Name the parasite shown.
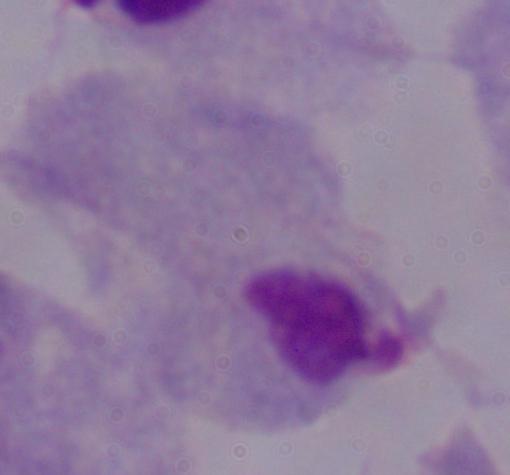
This is a trichomonad.

Captured at 1000x magnification. Photomicrograph.